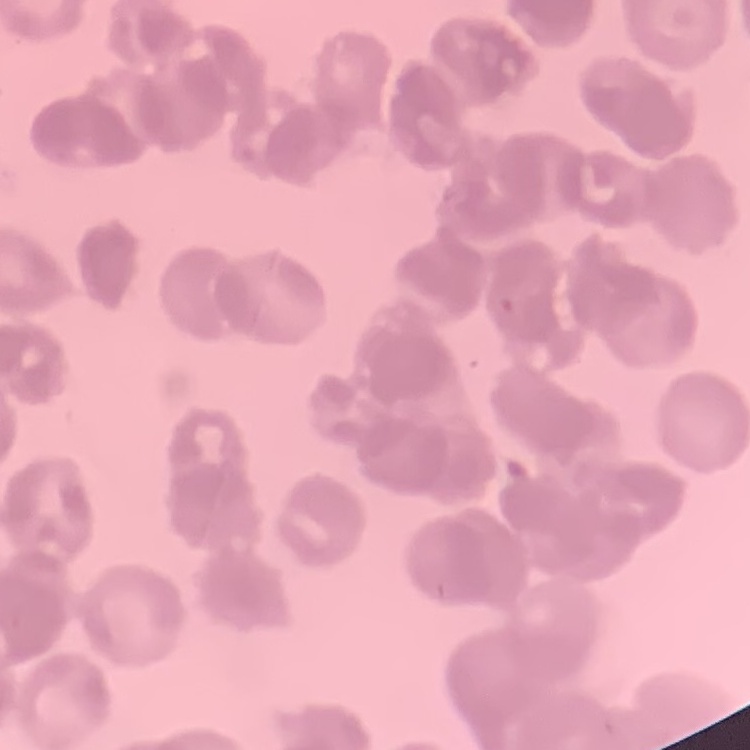

Summary:
  - Erythrocyte morphology: rouleaux formation
  - Preparation: thin peripheral smear
  - Stain: Field's or Giemsa
  - Image type: square crop of a larger photomicrograph